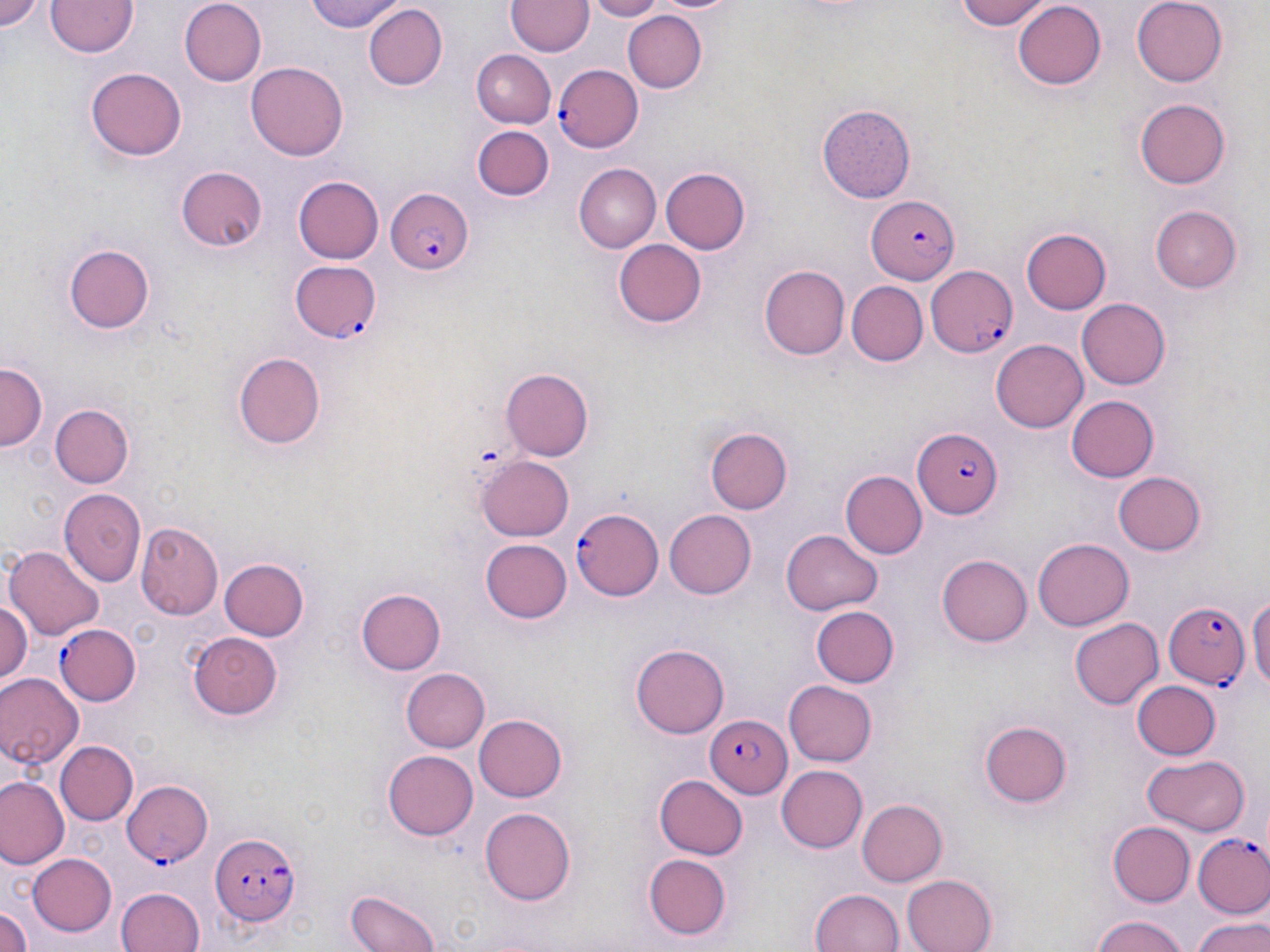 Approximate bounding boxes as named x1/y1/x2/y2 corners in pixels. Plasmodium falciparum-infected red blood cell locations: (x1=553, y1=63, x2=643, y2=153), (x1=385, y1=186, x2=474, y2=277), (x1=865, y1=195, x2=958, y2=282), (x1=290, y1=262, x2=381, y2=343), (x1=924, y1=266, x2=1020, y2=356), (x1=914, y1=430, x2=1004, y2=517), (x1=571, y1=509, x2=662, y2=601), (x1=1164, y1=602, x2=1250, y2=692), (x1=55, y1=623, x2=141, y2=706), (x1=706, y1=714, x2=794, y2=796), (x1=121, y1=780, x2=212, y2=868), (x1=213, y1=832, x2=303, y2=924), (x1=1195, y1=833, x2=1270, y2=918). Uninfected red blood cell locations: (x1=0, y1=0, x2=49, y2=39), (x1=46, y1=0, x2=138, y2=60), (x1=304, y1=0, x2=406, y2=34), (x1=583, y1=0, x2=669, y2=21), (x1=951, y1=0, x2=1049, y2=30), (x1=1132, y1=0, x2=1229, y2=87), (x1=181, y1=1, x2=267, y2=85), (x1=507, y1=1, x2=592, y2=57), (x1=1011, y1=2, x2=1105, y2=91), (x1=363, y1=4, x2=446, y2=88), (x1=622, y1=9, x2=706, y2=94), (x1=471, y1=51, x2=555, y2=127), (x1=247, y1=58, x2=346, y2=158), (x1=87, y1=64, x2=185, y2=159), (x1=1135, y1=96, x2=1230, y2=187), (x1=818, y1=105, x2=914, y2=203), (x1=472, y1=125, x2=555, y2=202), (x1=574, y1=164, x2=660, y2=252), (x1=174, y1=166, x2=269, y2=251), (x1=661, y1=167, x2=750, y2=255), (x1=294, y1=177, x2=383, y2=265), (x1=1151, y1=205, x2=1243, y2=291), (x1=1022, y1=228, x2=1111, y2=314), (x1=613, y1=238, x2=706, y2=326), (x1=63, y1=244, x2=156, y2=334), (x1=759, y1=265, x2=848, y2=360), (x1=845, y1=282, x2=926, y2=366), (x1=1077, y1=298, x2=1172, y2=389), (x1=992, y1=340, x2=1089, y2=432), (x1=230, y1=350, x2=328, y2=450), (x1=0, y1=363, x2=45, y2=453), (x1=501, y1=367, x2=594, y2=461), (x1=1067, y1=395, x2=1162, y2=482), (x1=46, y1=403, x2=137, y2=488), (x1=708, y1=428, x2=792, y2=514), (x1=479, y1=454, x2=576, y2=541), (x1=839, y1=469, x2=926, y2=559), (x1=1114, y1=470, x2=1207, y2=554), (x1=58, y1=487, x2=146, y2=587), (x1=662, y1=510, x2=754, y2=599), (x1=137, y1=522, x2=223, y2=619), (x1=781, y1=529, x2=885, y2=614), (x1=483, y1=538, x2=572, y2=623), (x1=1034, y1=538, x2=1134, y2=632), (x1=7, y1=544, x2=104, y2=639), (x1=937, y1=554, x2=1034, y2=647), (x1=219, y1=556, x2=311, y2=642), (x1=357, y1=589, x2=446, y2=676), (x1=1249, y1=591, x2=1270, y2=698), (x1=0, y1=600, x2=31, y2=684), (x1=810, y1=605, x2=899, y2=687), (x1=1070, y1=617, x2=1162, y2=710), (x1=186, y1=632, x2=284, y2=720), (x1=630, y1=643, x2=729, y2=738), (x1=402, y1=668, x2=492, y2=753), (x1=0, y1=672, x2=83, y2=769), (x1=1134, y1=678, x2=1222, y2=759), (x1=784, y1=680, x2=876, y2=766), (x1=474, y1=714, x2=569, y2=802), (x1=979, y1=720, x2=1073, y2=809), (x1=57, y1=740, x2=136, y2=825), (x1=383, y1=750, x2=479, y2=841), (x1=1141, y1=753, x2=1252, y2=834), (x1=775, y1=765, x2=867, y2=853), (x1=656, y1=773, x2=750, y2=859), (x1=1, y1=778, x2=67, y2=869), (x1=858, y1=799, x2=948, y2=884), (x1=479, y1=807, x2=578, y2=905), (x1=1108, y1=821, x2=1195, y2=904), (x1=26, y1=851, x2=117, y2=936), (x1=645, y1=854, x2=732, y2=939), (x1=901, y1=872, x2=996, y2=952), (x1=114, y1=885, x2=206, y2=952), (x1=809, y1=886, x2=905, y2=952), (x1=345, y1=887, x2=443, y2=952), (x1=0, y1=901, x2=34, y2=952), (x1=1191, y1=912, x2=1270, y2=952), (x1=1089, y1=914, x2=1193, y2=952). Slide-level diagnosis: Plasmodium falciparum. May-Grünwald-Giemsa stain. Single field of view. 1000x magnification. Optical microscopy. Image is 1270×952 pixels. Thin blood smear.